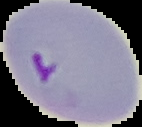 Image is 142×127 pixels. Segmented cell region on a black background. Malaria status: parasitized. From a thin blood film.